Identify the parasite.
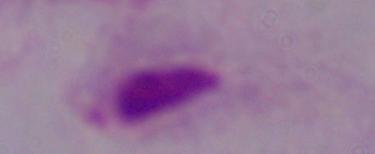
This is a trichomonad.

Micrograph. 1000x magnification.